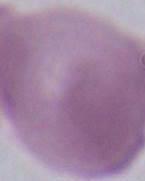

Micrograph. An erythrocyte is seen. Captured at 1000x magnification.